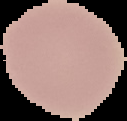
Summary:
  - Result: no Plasmodium parasites detected
  - Preparation: thin blood smear
  - Image type: segmented cell region on a black background
  - Image size: 127×121 pixels